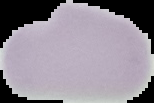

Summary:
  - Image size: 154×103 pixels
  - Image type: cell region segmented out of the field of view; surrounding area masked to black
  - Preparation: thin blood film
  - Malaria status: uninfected